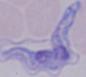
{
  "modality": "photomicrograph",
  "identification": "trypanosome",
  "magnification": "1000x"
}